Outline each blood parasite and name the species.
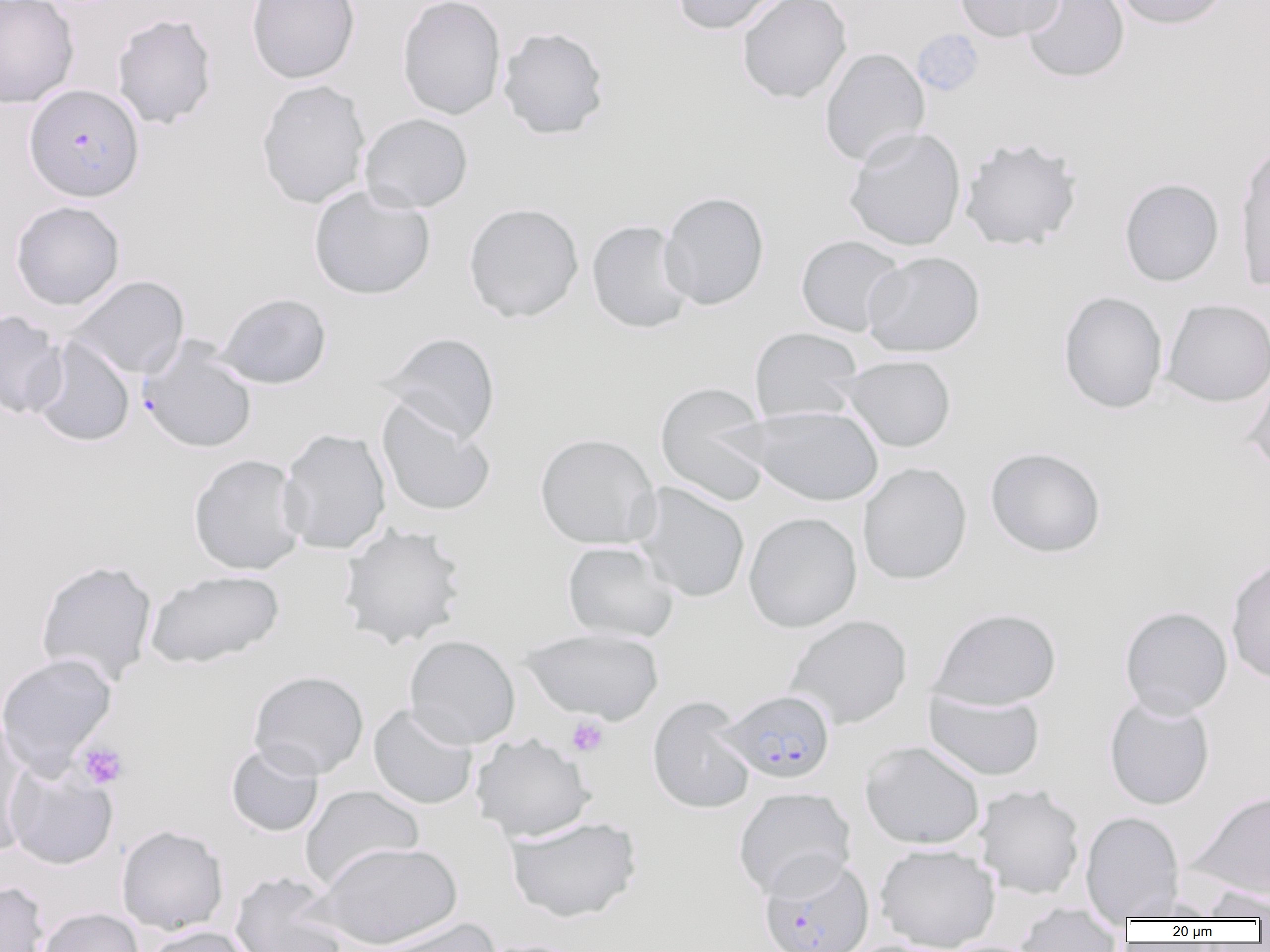
Approximate bounding boxes as [x1, y1, x2, y2] in pixels.
Plasmodium falciparum-infected red blood cells: [24, 84, 144, 202], [137, 337, 258, 455], [719, 689, 836, 783], [759, 854, 874, 952].
No Plasmodium ovale, Plasmodium malariae, Plasmodium vivax, Babesia divergens, or Trypanosoma brucei observed.

Platelet locations: [912, 29, 985, 97], [566, 716, 609, 758], [78, 742, 128, 789]. Uninfected red blood cell locations: [0, 0, 79, 107], [246, 0, 360, 84], [397, 0, 506, 120], [672, 0, 787, 35], [736, 0, 852, 103], [954, 0, 1065, 42], [1021, 0, 1130, 83], [1112, 0, 1230, 29], [111, 14, 217, 129], [497, 26, 610, 140], [819, 47, 930, 167], [256, 80, 370, 209], [360, 113, 473, 213], [844, 127, 966, 251], [959, 138, 1082, 251], [1235, 139, 1270, 294], [1119, 178, 1224, 286], [308, 184, 436, 300], [659, 191, 769, 310], [10, 200, 126, 311], [463, 203, 584, 323], [587, 220, 694, 334], [795, 234, 907, 337], [861, 250, 985, 358], [67, 275, 189, 379], [1058, 290, 1168, 414], [216, 292, 332, 389], [1162, 298, 1270, 407], [0, 310, 67, 420], [749, 327, 864, 425], [378, 331, 501, 443], [30, 337, 135, 448], [838, 354, 957, 452], [1244, 369, 1270, 476], [654, 382, 773, 506], [376, 399, 496, 517], [741, 404, 884, 507], [278, 427, 392, 555], [534, 432, 661, 549], [985, 447, 1106, 558], [188, 453, 306, 575], [858, 462, 972, 585], [633, 482, 751, 603], [743, 511, 862, 633], [338, 523, 467, 649], [562, 541, 678, 642], [1225, 557, 1270, 685], [34, 559, 158, 687], [145, 569, 284, 669], [1119, 606, 1233, 719], [929, 607, 1062, 710], [785, 614, 912, 729], [522, 627, 664, 724], [404, 634, 520, 749], [0, 652, 118, 775], [248, 670, 369, 779], [923, 687, 1045, 782], [1103, 694, 1215, 810], [647, 696, 756, 814], [367, 703, 479, 809], [0, 713, 35, 855], [471, 733, 594, 841], [860, 740, 985, 850], [225, 742, 324, 837], [4, 762, 118, 870], [974, 784, 1085, 899], [300, 785, 424, 890], [733, 786, 856, 899], [1191, 789, 1270, 902], [1080, 811, 1184, 920], [505, 815, 642, 923], [116, 824, 229, 935], [317, 841, 461, 949], [874, 843, 1000, 952], [229, 872, 348, 952], [0, 881, 50, 952], [1200, 887, 1270, 921], [1118, 896, 1224, 921], [1014, 904, 1124, 952], [37, 907, 144, 952], [372, 917, 500, 952], [140, 925, 258, 952], [837, 938, 960, 952], [476, 939, 592, 952]. Slide-level diagnosis: Plasmodium falciparum. Captured at 1000x magnification. Image is 1270×952 pixels. Single field of view. Thin blood film. Light microscopy.